Assess this cell for malaria.
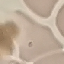
It is uninfected.

Giemsa stain. Cell patch, automatically extracted from a larger field of view and resized to 64 × 64 pixels. Acquired by smartphone through the microscope eyepiece. Thin blood film.